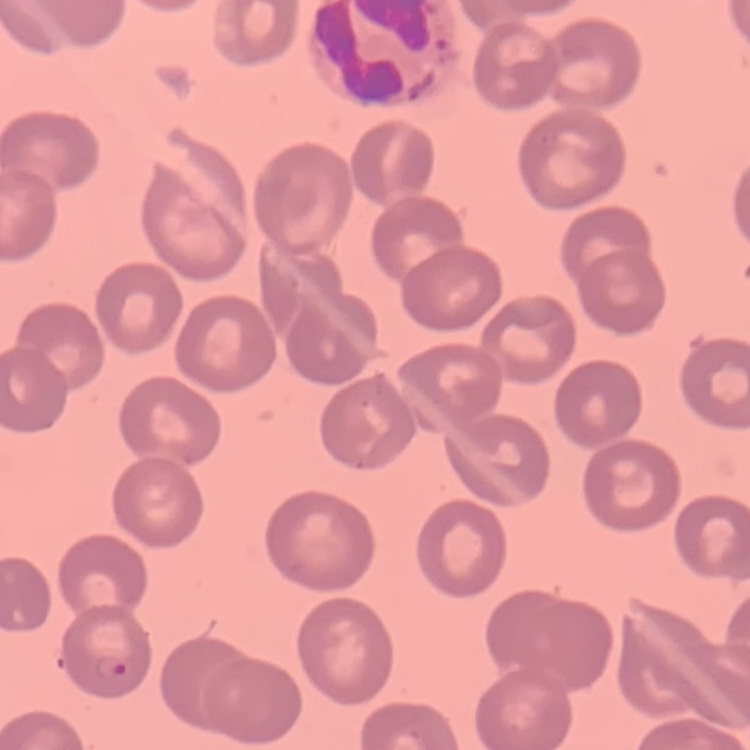
Summary:
  - Erythrocyte morphology: no rouleaux formation
  - Image type: square crop of a larger photomicrograph
  - Preparation: thin blood film
  - Stain: Field's or Giemsa